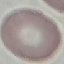
Summary:
  - Result: no malaria parasites detected
  - Capture: smartphone camera at the microscope eyepiece
  - Preparation: thin smear
  - Stain: Giemsa
  - Image type: cell patch, automatically extracted from a larger field of view and resized to 64 × 64 pixels